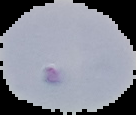
Image is 136×115 pixels. Result: Plasmodium parasites identified. From a thin blood smear. Segmented cell region on a black background.